Assess the morphology of the red blood cells.
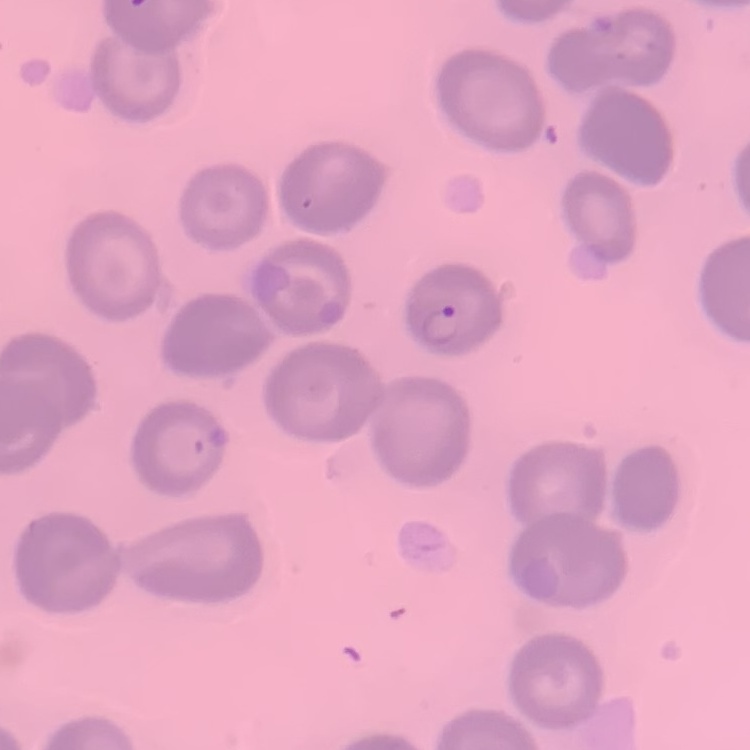
No rouleaux formation.

image_type: one tile cut from a larger photomicrograph
preparation: thin peripheral smear
stain: Field's or Giemsa